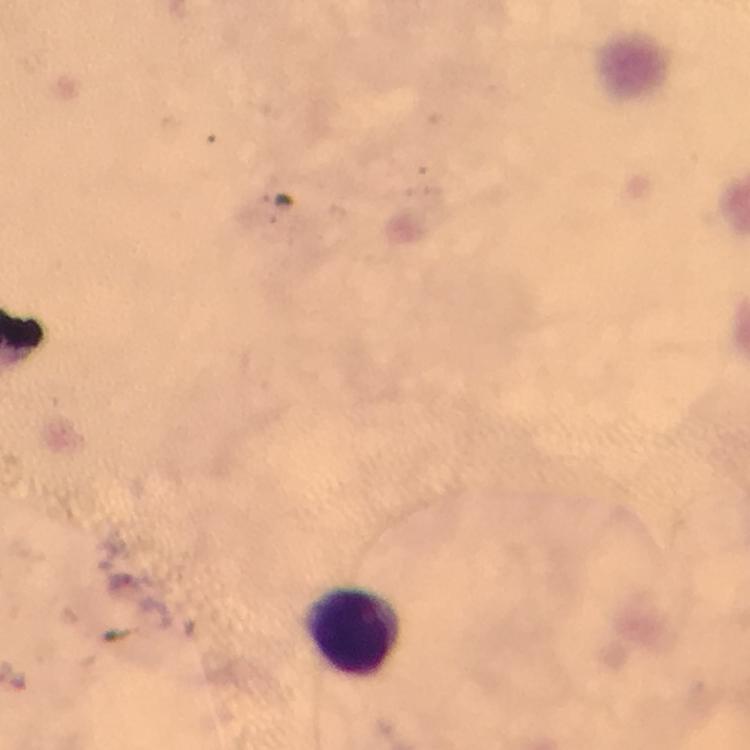

context = from a diagnostic examination for malaria
magnification = 100x
immersion oil = used
preparation = thick blood film
leukocyte locations = approximate object centers, in pixels from the top-left corner: (x=354, y=629)
stain = Giemsa
Plasmodium parasite locations = approximate object centers, in pixels from the top-left corner: (x=120, y=582)
capture = smartphone camera through the microscope
image size = 750×750 pixels
cropped from = a single field of view